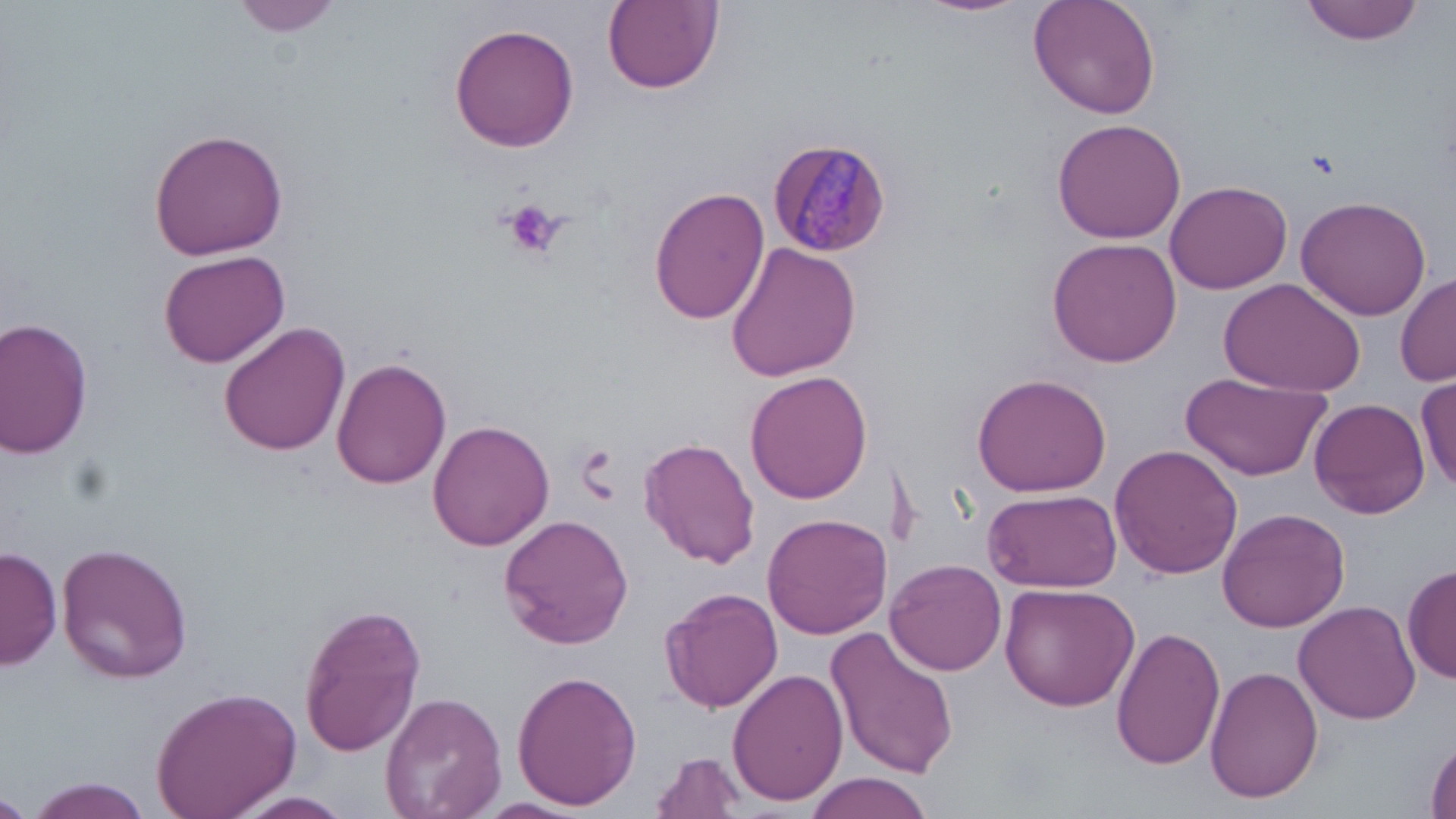
slide-level diagnosis = Plasmodium malariae
image size = 1456×819 pixels
field of view = single
magnification = 1000x
preparation = thin blood smear
platelet locations = approximate bounding boxes as (x1, y1, x2, y2) in pixels: (503, 200, 566, 259)
Plasmodium malariae-infected red blood cell locations = approximate bounding boxes as (x1, y1, x2, y2) in pixels: (767, 136, 891, 260)
modality = light microscopy
uninfected red blood cell locations = approximate bounding boxes as (x1, y1, x2, y2) in pixels: (233, 0, 343, 36), (920, 0, 1029, 17), (1029, 0, 1162, 121), (1299, 0, 1427, 44), (602, 1, 722, 93), (450, 23, 580, 154), (1052, 118, 1186, 244), (147, 128, 290, 259), (1165, 180, 1293, 294), (648, 184, 770, 327), (1295, 194, 1432, 320), (1047, 238, 1182, 367), (725, 240, 863, 382), (159, 249, 290, 368), (1397, 273, 1456, 386), (1219, 277, 1366, 396), (1, 317, 97, 459), (218, 321, 350, 454), (332, 357, 452, 488), (744, 370, 873, 503), (972, 371, 1113, 498), (1182, 371, 1331, 482), (1416, 374, 1456, 493), (1310, 399, 1430, 518), (428, 420, 553, 551), (639, 439, 761, 570), (1110, 443, 1244, 580), (984, 488, 1123, 593), (1217, 506, 1350, 632), (500, 514, 634, 649), (762, 514, 893, 640), (57, 541, 193, 685), (1, 545, 62, 670), (888, 558, 1007, 676), (1404, 562, 1456, 686), (1000, 583, 1139, 712), (659, 587, 783, 715), (1293, 599, 1422, 723), (300, 602, 427, 757), (825, 626, 958, 781), (1110, 626, 1226, 770), (1204, 663, 1324, 802), (728, 668, 850, 807), (511, 669, 641, 810), (150, 684, 300, 819), (379, 690, 506, 819), (1426, 737, 1456, 819), (650, 751, 746, 818), (804, 774, 931, 818), (21, 777, 156, 819), (228, 791, 357, 818), (0, 795, 25, 819)
stain = May-Grünwald-Giemsa